Name the blood parasite species.
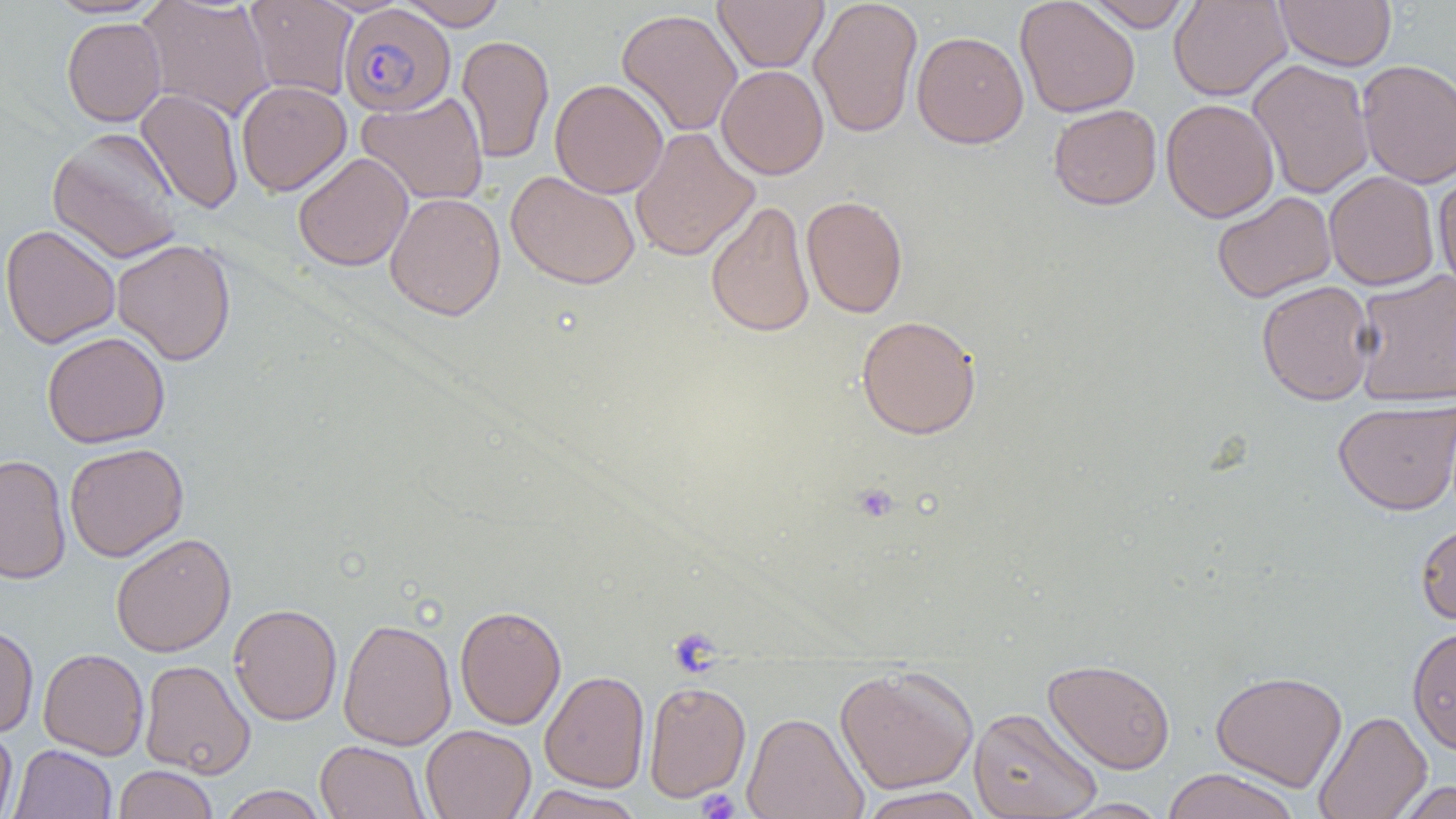

Plasmodium falciparum.

Approximate bounding boxes as named x1/y1/x2/y2 corners in pixels. Plasmodium falciparum-infected red blood cell locations: (x1=339, y1=4, x2=455, y2=117). Platelet locations: (x1=851, y1=483, x2=900, y2=523), (x1=697, y1=788, x2=740, y2=818). Uninfected red blood cell locations: (x1=44, y1=0, x2=165, y2=18), (x1=136, y1=0, x2=274, y2=121), (x1=244, y1=0, x2=358, y2=100), (x1=398, y1=0, x2=508, y2=30), (x1=713, y1=0, x2=828, y2=73), (x1=808, y1=0, x2=923, y2=139), (x1=1015, y1=0, x2=1140, y2=118), (x1=1083, y1=0, x2=1193, y2=32), (x1=1168, y1=0, x2=1293, y2=101), (x1=1274, y1=0, x2=1397, y2=71), (x1=616, y1=8, x2=743, y2=137), (x1=61, y1=17, x2=167, y2=127), (x1=911, y1=30, x2=1029, y2=148), (x1=456, y1=35, x2=554, y2=163), (x1=1247, y1=59, x2=1375, y2=199), (x1=1356, y1=59, x2=1456, y2=188), (x1=716, y1=64, x2=829, y2=180), (x1=550, y1=79, x2=669, y2=198), (x1=236, y1=80, x2=351, y2=196), (x1=135, y1=89, x2=244, y2=214), (x1=356, y1=91, x2=489, y2=206), (x1=1161, y1=98, x2=1279, y2=222), (x1=1048, y1=104, x2=1162, y2=210), (x1=630, y1=127, x2=759, y2=262), (x1=47, y1=128, x2=184, y2=264), (x1=293, y1=152, x2=413, y2=271), (x1=1433, y1=167, x2=1456, y2=297), (x1=506, y1=170, x2=640, y2=289), (x1=1324, y1=171, x2=1440, y2=291), (x1=1211, y1=191, x2=1336, y2=303), (x1=385, y1=192, x2=506, y2=321), (x1=801, y1=195, x2=908, y2=318), (x1=705, y1=201, x2=816, y2=338), (x1=1, y1=224, x2=120, y2=349), (x1=112, y1=238, x2=236, y2=365), (x1=1353, y1=269, x2=1456, y2=406), (x1=1256, y1=280, x2=1377, y2=406), (x1=856, y1=314, x2=982, y2=439), (x1=42, y1=331, x2=170, y2=448), (x1=1332, y1=399, x2=1456, y2=515), (x1=64, y1=442, x2=189, y2=562), (x1=0, y1=455, x2=71, y2=585), (x1=1415, y1=518, x2=1456, y2=627), (x1=111, y1=532, x2=236, y2=657), (x1=228, y1=603, x2=343, y2=726), (x1=454, y1=604, x2=567, y2=730), (x1=338, y1=617, x2=457, y2=751), (x1=0, y1=623, x2=38, y2=738), (x1=1407, y1=625, x2=1456, y2=755), (x1=38, y1=648, x2=149, y2=760), (x1=1043, y1=658, x2=1176, y2=774), (x1=140, y1=659, x2=255, y2=778), (x1=834, y1=665, x2=979, y2=794), (x1=1210, y1=669, x2=1348, y2=791), (x1=539, y1=670, x2=650, y2=793), (x1=643, y1=680, x2=751, y2=803), (x1=641, y1=694, x2=863, y2=809), (x1=968, y1=706, x2=1103, y2=819), (x1=1313, y1=710, x2=1432, y2=819), (x1=742, y1=711, x2=869, y2=819), (x1=0, y1=724, x2=18, y2=819), (x1=420, y1=725, x2=536, y2=819), (x1=315, y1=740, x2=428, y2=819), (x1=9, y1=744, x2=116, y2=819), (x1=113, y1=765, x2=218, y2=819), (x1=1160, y1=768, x2=1301, y2=819), (x1=1394, y1=780, x2=1454, y2=818), (x1=218, y1=785, x2=329, y2=819), (x1=521, y1=785, x2=645, y2=819), (x1=857, y1=786, x2=987, y2=819), (x1=1052, y1=797, x2=1173, y2=818). Image is 1456×819 pixels. One field of a larger specimen. 1000x magnification. Thin blood smear. Optical microscopy.